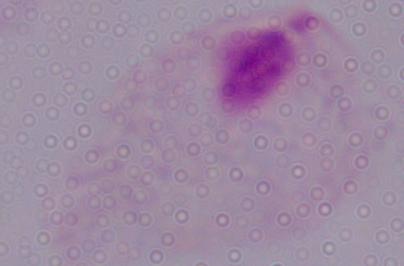
Micrograph. Captured at 1000x magnification. A trichomonad is seen.